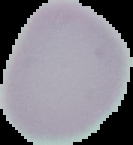

Summary:
  - Result: negative for Plasmodium parasites
  - Image type: segmented cell region with the area outside set to black
  - Preparation: thin blood smear
  - Image size: 133×145 pixels